Point out each Plasmodium parasite.
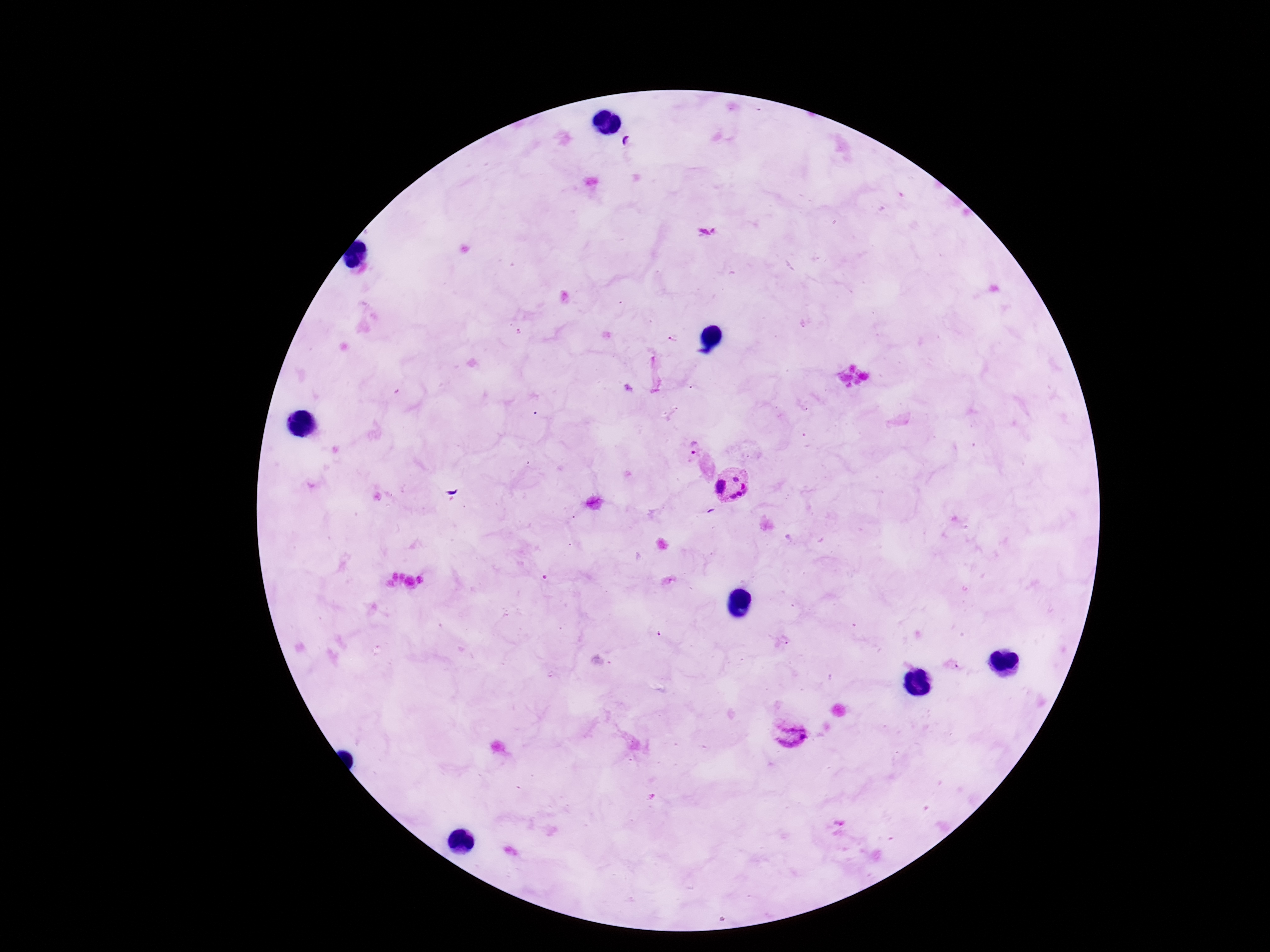
Approximate centers as {x, y} in pixels.
Plasmodium parasites: {706, 232}, {693, 447}, {731, 484}, {789, 733}.

field of view = one from this slide
magnification = 100x
stain = Giemsa
preparation = thick blood film
capture = smartphone camera through the microscope eyepiece
patient malaria status = infected
image size = 1270×952 pixels